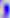
Summary:
  - Modality: micrograph
  - Identification: Toxoplasma gondii
  - Magnification: 400x